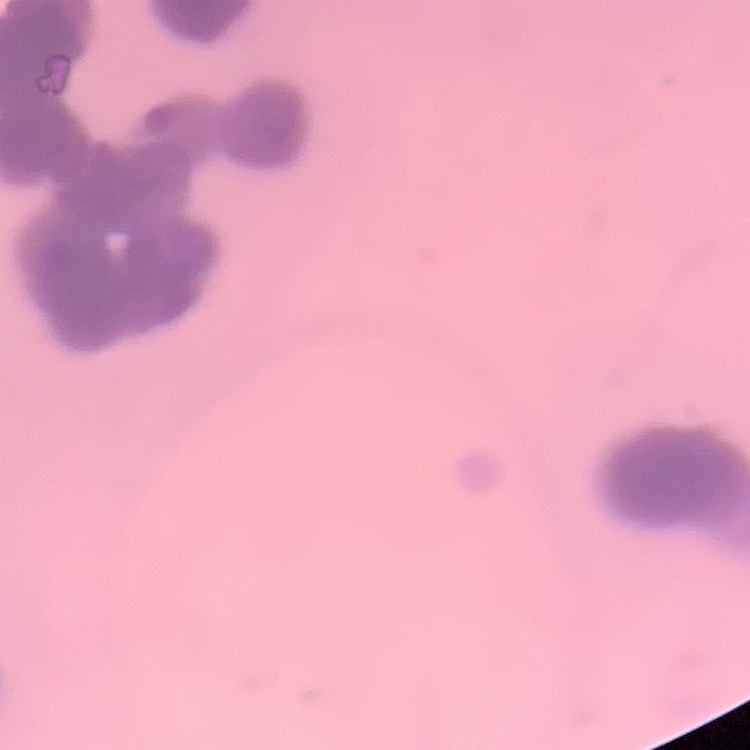

Summary:
  - Red blood cell morphology: rouleaux formation
  - Preparation: thin peripheral smear
  - Image type: square crop of a larger photomicrograph
  - Stain: Field's or Giemsa